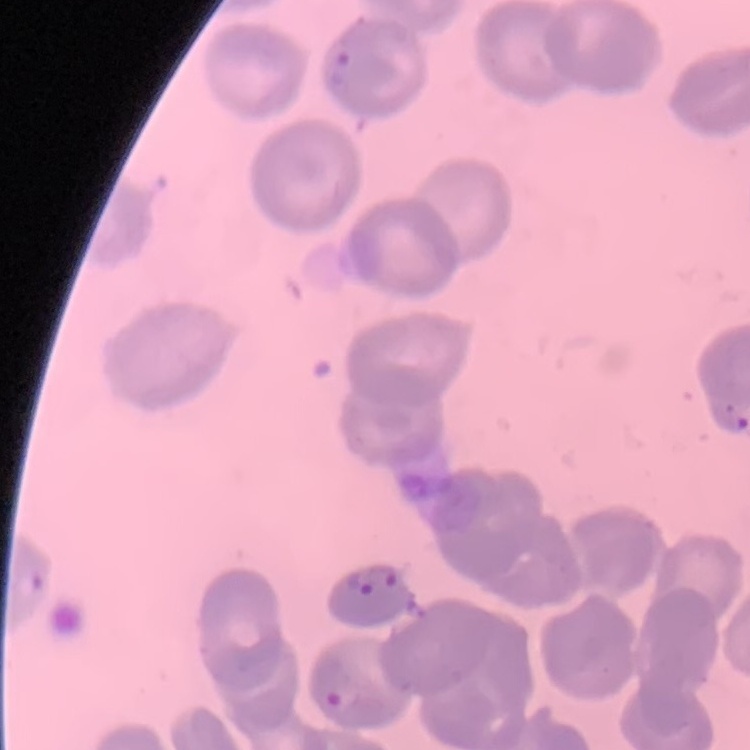

{
  "red_blood_cell_morphology": "no rouleaux formation",
  "preparation": "thin peripheral smear",
  "image_type": "square crop of a larger photomicrograph",
  "stain": "Field's or Giemsa"
}